Classify this cell by malaria status.
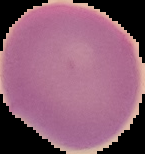
Uninfected.

preparation = thin blood smear
image type = segmented cell region with the area outside set to black
image size = 145×154 pixels